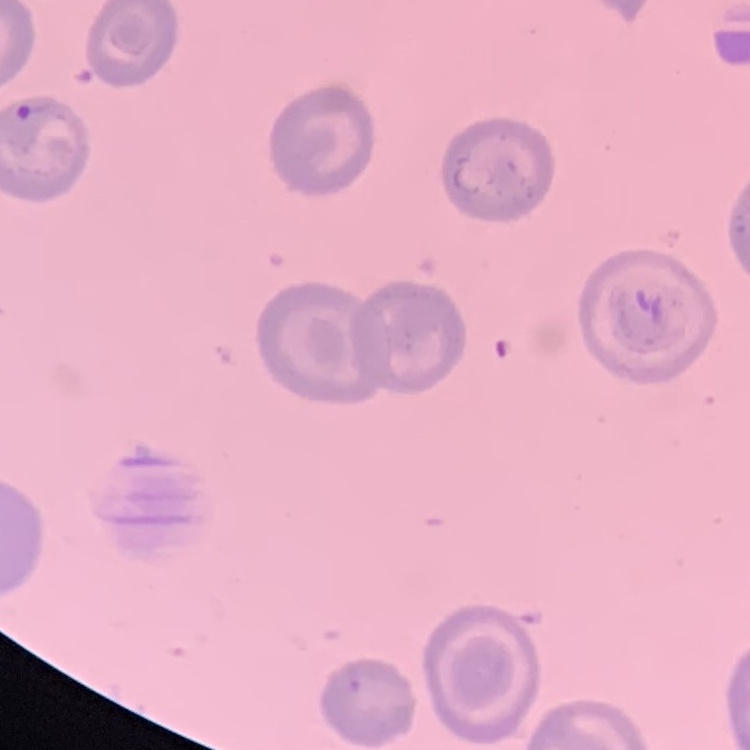

The erythrocytes show no rouleaux formation. Stained with either Field's or Giemsa. Thin blood film. One tile cut from a larger photomicrograph.